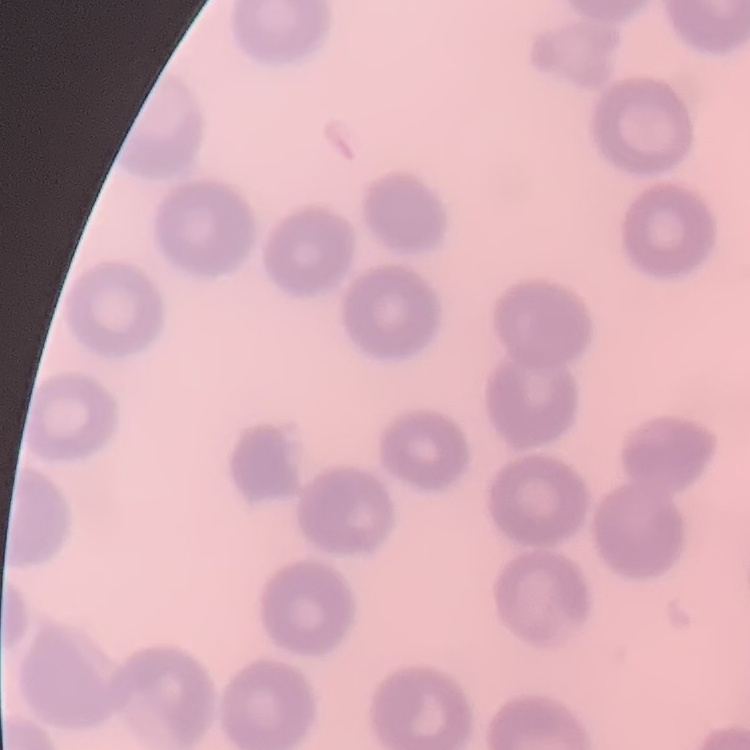

Summary:
  - Erythrocyte morphology: no rouleaux formation
  - Preparation: thin blood film
  - Stain: Field's or Giemsa
  - Image type: one tile cut from a larger photomicrograph